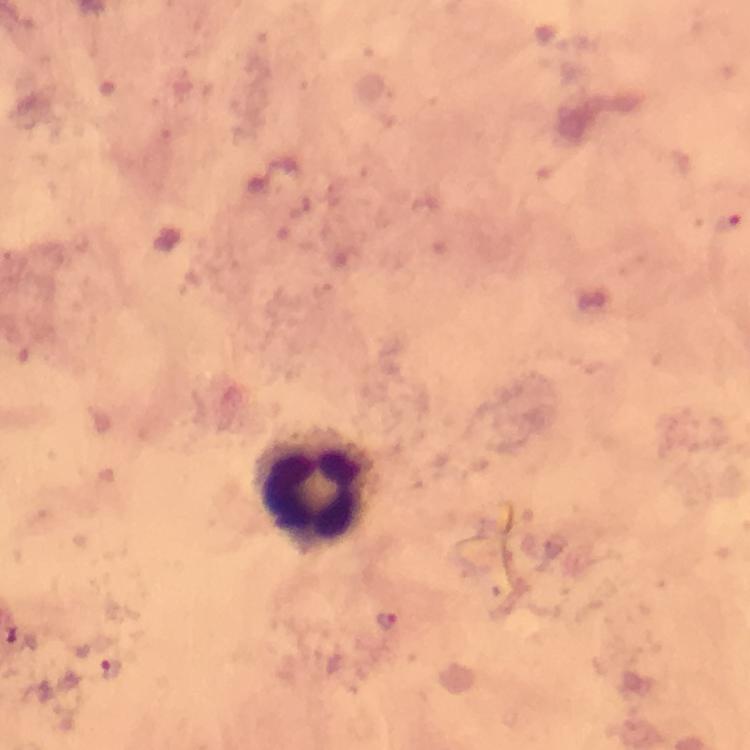
Approximate centers as {x, y} in pixels. Malaria parasite locations: {726, 221}, {387, 622}, {111, 668}. Leukocyte locations: {311, 492}. At 100x magnification. Image is 750×750 pixels. From a diagnostic examination for malaria. A crop from one field of view. Photographed with a smartphone mounted on the microscope. Thick smear. Immersion oil applied. Giemsa-stained preparation.